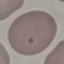

malaria status = uninfected
stain = Giemsa
capture = smartphone through the microscope eyepiece
image type = cell patch, automatically extracted from a larger field of view and resized to 64 × 64 pixels
preparation = thin blood film